Classify this cell by malaria status.
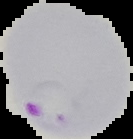
Parasitized.

Image is 133×139 pixels. From a thin blood smear. The area outside the segmented cell region is set to black.